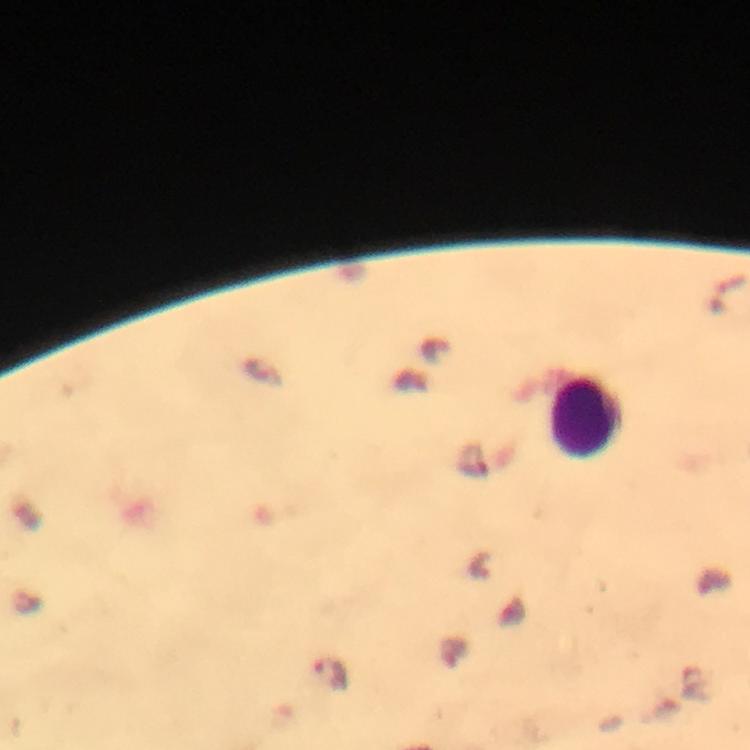
Approximate centers as {x, y} in pixels. Malaria parasite locations: {330, 673}. Leukocyte locations: {585, 417}. Giemsa-stained preparation. 100x magnification. Photographed through the microscope with a smartphone camera. Immersion oil was used. Image is 750×750 pixels. Cropped region of a single field of view. From a diagnostic examination for malaria. Thick blood film.